Classify this cell by malaria status.
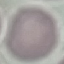
It is uninfected.

Summary:
  - Stain: Giemsa
  - Capture: smartphone camera at the microscope eyepiece
  - Preparation: thin blood smear
  - Image type: automatically extracted cell patch, resized to 64 × 64 pixels